Name the parasite shown.
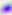

Toxoplasma gondii.

Summary:
  - Modality: micrograph
  - Magnification: 400x